Locate and identify every blood parasite.
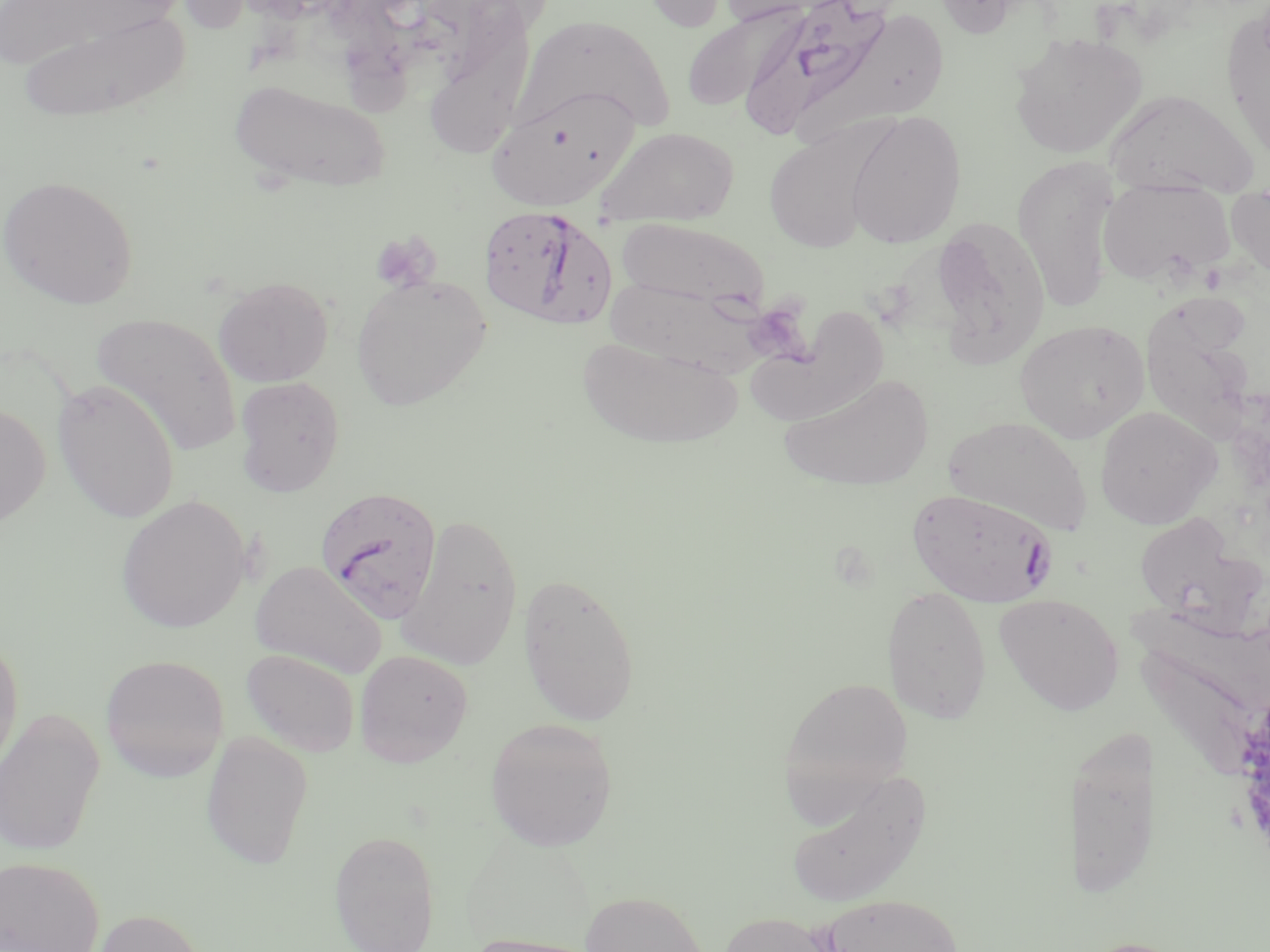
Approximate bounding boxes as [x1, y1, x2, y2] in pixels.
Plasmodium falciparum-infected red blood cells: [737, 0, 903, 140], [478, 206, 617, 331], [316, 484, 442, 621], [906, 488, 1059, 606].
No Plasmodium ovale, Plasmodium malariae, Plasmodium vivax, Babesia divergens, or Trypanosoma brucei observed.

Summary:
  - Platelet locations: [372, 232, 440, 291], [752, 309, 818, 370]
  - Uninfected red blood cell locations: [634, 0, 734, 33], [712, 0, 838, 27], [931, 0, 1027, 38], [429, 6, 510, 157], [681, 7, 801, 111], [15, 8, 190, 123], [1220, 9, 1270, 165], [516, 14, 677, 135], [1009, 30, 1148, 160], [229, 77, 392, 195], [487, 86, 638, 211], [1104, 88, 1260, 197], [844, 110, 966, 249], [597, 126, 739, 226], [764, 131, 876, 253], [1012, 154, 1121, 310], [1, 174, 138, 309], [1097, 179, 1233, 287], [1227, 189, 1270, 280], [928, 215, 1050, 369], [616, 218, 769, 315], [350, 273, 491, 411], [606, 274, 770, 378], [213, 275, 333, 387], [1138, 295, 1260, 444], [744, 310, 895, 425], [92, 312, 242, 456], [1014, 319, 1150, 443], [576, 335, 744, 449], [777, 372, 935, 493], [234, 375, 345, 497], [52, 379, 181, 524], [0, 401, 50, 528], [1095, 406, 1221, 529], [945, 416, 1091, 535], [116, 494, 251, 633], [1133, 510, 1259, 628], [398, 513, 523, 669], [250, 560, 385, 677], [517, 572, 641, 726], [882, 586, 992, 726], [994, 594, 1125, 716], [1130, 596, 1270, 708], [0, 632, 24, 782], [240, 648, 360, 757], [354, 649, 473, 767], [1137, 653, 1270, 785], [100, 654, 228, 782], [779, 675, 913, 808], [0, 707, 105, 857], [484, 717, 619, 851], [200, 730, 314, 868], [1072, 731, 1152, 899], [785, 768, 930, 908], [328, 830, 439, 952], [1, 856, 104, 952], [579, 891, 709, 952], [819, 893, 965, 952], [93, 908, 207, 952], [718, 911, 839, 952], [462, 931, 603, 952], [1074, 937, 1197, 952]
  - Slide-level diagnosis: Plasmodium falciparum
  - Stain: May-Grünwald-Giemsa
  - Image size: 1270×952 pixels
  - Field of view: one of a larger specimen
  - Modality: light microscopy
  - Preparation: thin blood film
  - Magnification: 1000x